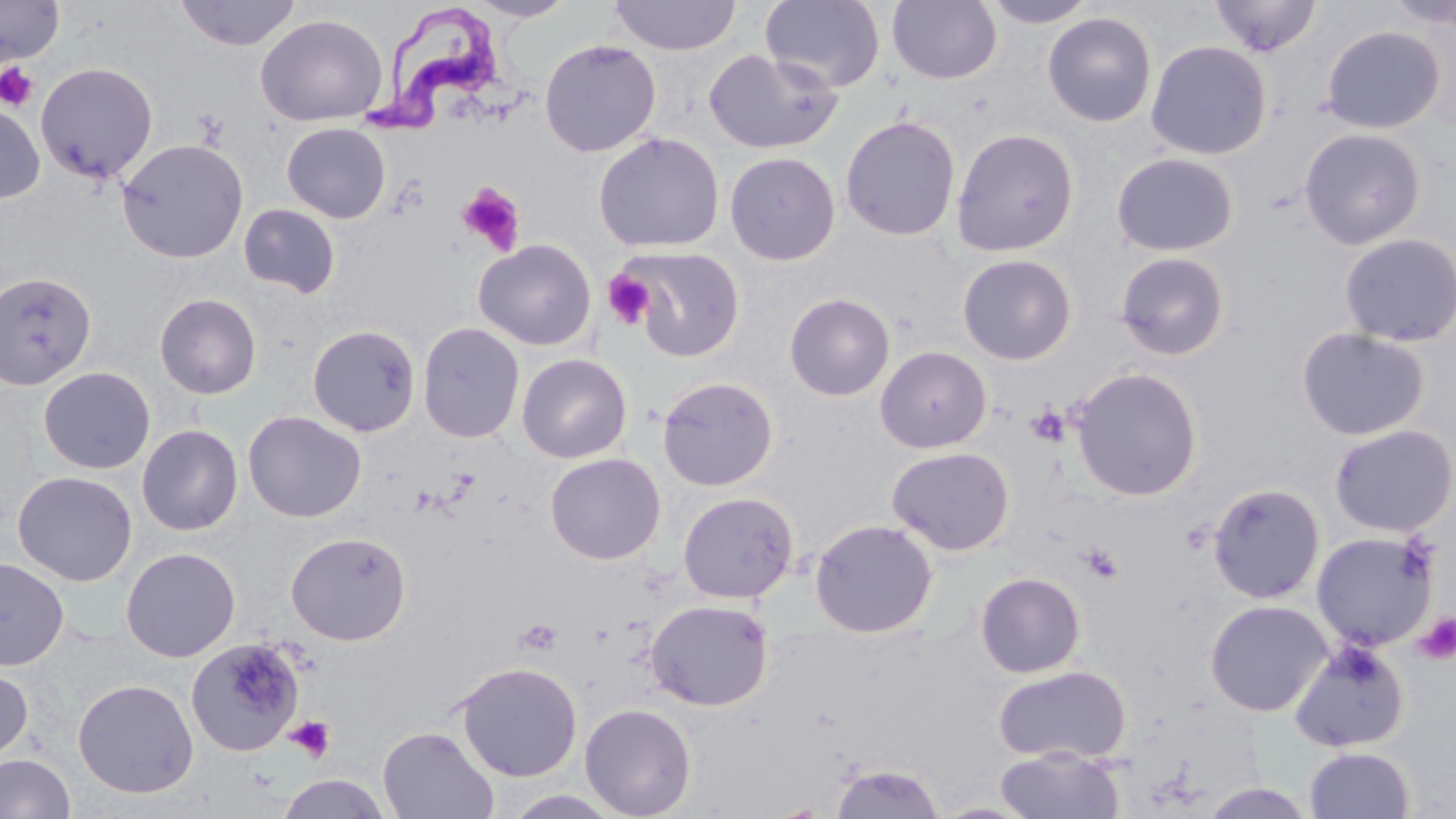
slide-level diagnosis = Trypanosoma brucei
modality = light microscopy
field of view = single
stain = May-Grünwald-Giemsa
uninfected red blood cell locations = approximate bounding boxes as [x1, y1, x2, y2] in pixels: [0, 0, 64, 65], [174, 0, 301, 51], [466, 0, 577, 22], [608, 0, 741, 56], [761, 0, 886, 93], [887, 0, 1002, 85], [980, 0, 1100, 28], [1208, 0, 1322, 57], [1042, 12, 1157, 127], [255, 13, 388, 127], [1320, 25, 1446, 134], [538, 38, 661, 157], [1145, 40, 1272, 160], [703, 48, 843, 155], [35, 61, 159, 183], [0, 103, 45, 204], [840, 115, 961, 241], [281, 123, 391, 223], [1298, 127, 1427, 250], [950, 128, 1080, 257], [592, 132, 724, 253], [115, 137, 250, 264], [724, 151, 841, 265], [1111, 152, 1239, 257], [238, 203, 342, 299], [1338, 232, 1456, 347], [473, 239, 596, 350], [622, 246, 745, 362], [1114, 250, 1231, 361], [957, 254, 1078, 365], [0, 270, 97, 392], [154, 293, 261, 399], [784, 293, 895, 401], [417, 322, 525, 443], [306, 324, 421, 437], [1295, 326, 1431, 441], [874, 346, 992, 453], [517, 353, 632, 463], [38, 366, 156, 474], [1069, 367, 1203, 501], [656, 376, 779, 491], [243, 410, 366, 523], [137, 424, 243, 536], [1328, 424, 1456, 537], [886, 446, 1015, 556], [544, 452, 666, 565], [12, 470, 137, 586], [1207, 482, 1325, 604], [677, 492, 799, 603], [809, 518, 938, 638], [285, 530, 411, 645], [1311, 530, 1439, 651], [120, 546, 241, 663], [0, 558, 69, 670], [975, 572, 1086, 678], [645, 599, 775, 712], [1204, 599, 1333, 717], [186, 637, 304, 756], [1289, 640, 1411, 753], [454, 661, 583, 782], [992, 664, 1132, 764], [0, 665, 33, 762], [72, 678, 198, 798], [579, 703, 697, 819], [378, 726, 499, 819], [1304, 746, 1415, 819], [994, 747, 1125, 819], [0, 753, 76, 819], [828, 760, 945, 818], [276, 772, 391, 819], [1197, 781, 1318, 819]
preparation = thin blood smear
platelet locations = approximate bounding boxes as [x1, y1, x2, y2] in pixels: [0, 62, 39, 111], [456, 182, 526, 256], [603, 270, 655, 330], [1026, 405, 1070, 446], [1082, 543, 1124, 583], [1415, 612, 1456, 664], [516, 618, 563, 657], [284, 714, 335, 764]
image size = 1456×819 pixels
Trypanosoma brucei locations = approximate bounding boxes as [x1, y1, x2, y2] in pixels: [359, 5, 503, 141]
magnification = 1000x